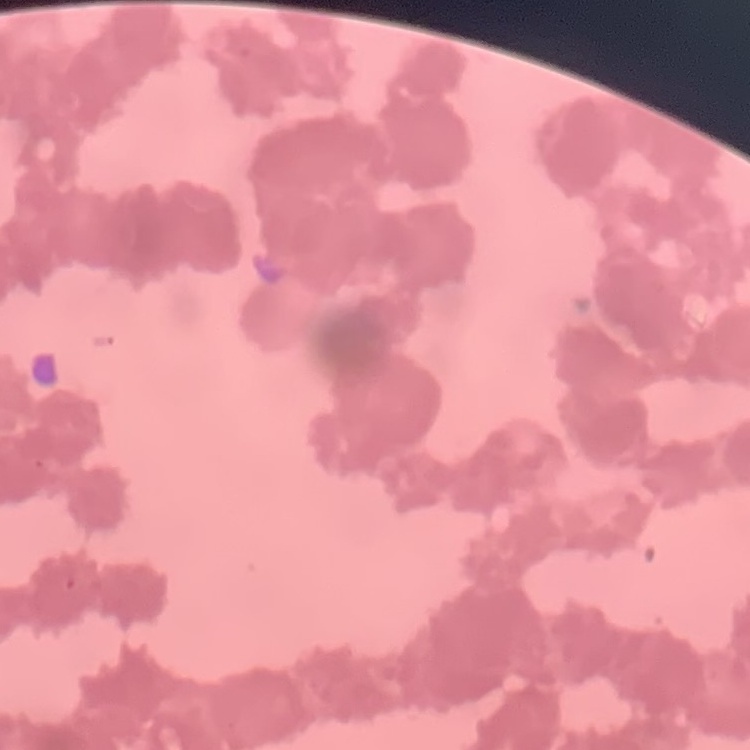

The red blood cells exhibit rouleaux formation. Field's or Giemsa stain. Square crop of a larger photomicrograph. Thin peripheral smear.